Assess this cell for malaria.
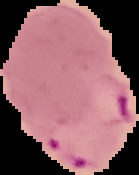
It is parasitized.

{
  "image_size": "139×175 pixels",
  "preparation": "thin blood smear",
  "image_type": "segmented cell region on a black background"
}